Assess this cell for malaria.
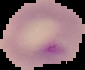

Parasitized.

Segmented cell region on a black background. From a thin blood film. Image is 85×70 pixels.